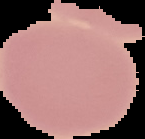

image size = 145×139 pixels
malaria status = uninfected
image type = segmented cell region with the area outside set to black
preparation = thin blood film